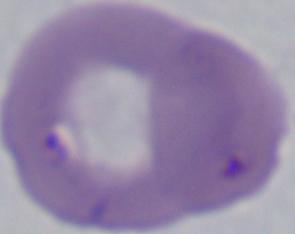
Summary:
  - Magnification: 1000x
  - Identification: Babesia
  - Modality: photomicrograph